Name the blood parasite species.
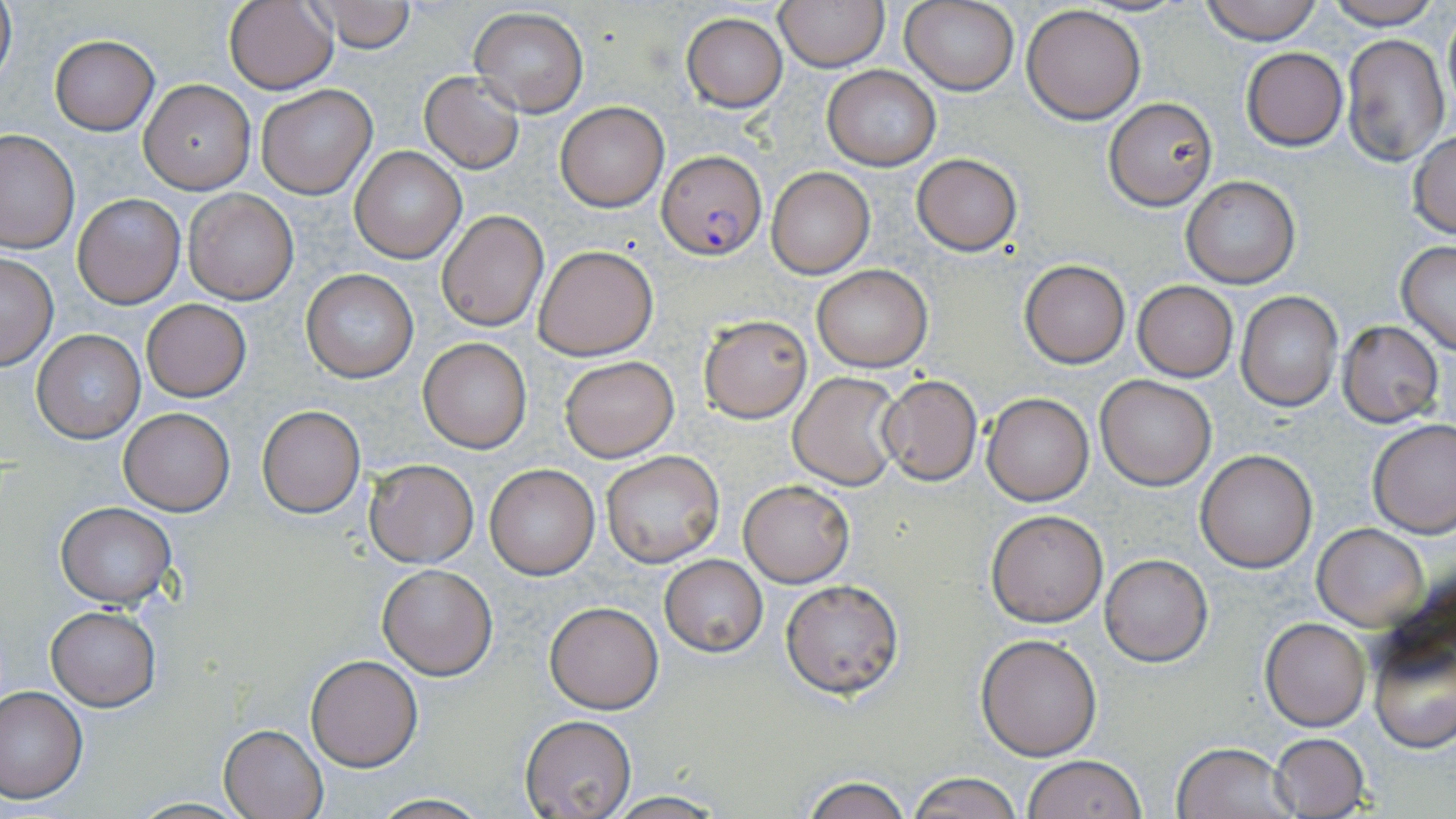
Plasmodium falciparum.

Approximate bounding boxes as named x1/y1/x2/y2 corners in pixels. Plasmodium falciparum-infected red blood cell locations: (x1=658, y1=149, x2=765, y2=260). Uninfected red blood cell locations: (x1=0, y1=0, x2=16, y2=90), (x1=223, y1=0, x2=339, y2=93), (x1=306, y1=0, x2=416, y2=52), (x1=774, y1=0, x2=889, y2=72), (x1=1198, y1=0, x2=1323, y2=44), (x1=1319, y1=0, x2=1442, y2=28), (x1=900, y1=1, x2=1019, y2=95), (x1=1022, y1=4, x2=1146, y2=123), (x1=469, y1=7, x2=589, y2=116), (x1=1441, y1=10, x2=1456, y2=115), (x1=680, y1=12, x2=788, y2=112), (x1=1340, y1=33, x2=1449, y2=166), (x1=50, y1=36, x2=158, y2=135), (x1=1241, y1=47, x2=1348, y2=150), (x1=822, y1=66, x2=942, y2=170), (x1=419, y1=71, x2=525, y2=174), (x1=140, y1=79, x2=256, y2=193), (x1=258, y1=84, x2=378, y2=199), (x1=1104, y1=98, x2=1217, y2=208), (x1=556, y1=102, x2=669, y2=212), (x1=0, y1=129, x2=78, y2=252), (x1=1407, y1=131, x2=1456, y2=237), (x1=349, y1=147, x2=466, y2=263), (x1=912, y1=154, x2=1020, y2=255), (x1=767, y1=167, x2=875, y2=278), (x1=1181, y1=175, x2=1300, y2=290), (x1=184, y1=189, x2=298, y2=304), (x1=73, y1=193, x2=184, y2=308), (x1=437, y1=210, x2=549, y2=331), (x1=1396, y1=241, x2=1456, y2=355), (x1=533, y1=244, x2=658, y2=359), (x1=0, y1=254, x2=58, y2=369), (x1=1021, y1=260, x2=1130, y2=367), (x1=812, y1=265, x2=931, y2=372), (x1=301, y1=269, x2=419, y2=383), (x1=1133, y1=281, x2=1238, y2=381), (x1=1236, y1=291, x2=1342, y2=411), (x1=141, y1=299, x2=251, y2=402), (x1=698, y1=314, x2=812, y2=423), (x1=1337, y1=322, x2=1442, y2=427), (x1=30, y1=329, x2=145, y2=444), (x1=418, y1=338, x2=532, y2=454), (x1=560, y1=356, x2=677, y2=461), (x1=789, y1=371, x2=903, y2=489), (x1=879, y1=375, x2=981, y2=486), (x1=1097, y1=375, x2=1217, y2=490), (x1=981, y1=392, x2=1094, y2=504), (x1=257, y1=404, x2=365, y2=518), (x1=119, y1=408, x2=234, y2=515), (x1=1368, y1=419, x2=1456, y2=537), (x1=1195, y1=450, x2=1318, y2=573), (x1=600, y1=451, x2=724, y2=567), (x1=364, y1=459, x2=479, y2=567), (x1=484, y1=463, x2=600, y2=580), (x1=740, y1=479, x2=853, y2=586), (x1=55, y1=502, x2=178, y2=606), (x1=985, y1=508, x2=1110, y2=628), (x1=1313, y1=523, x2=1429, y2=629), (x1=1100, y1=554, x2=1213, y2=667), (x1=660, y1=555, x2=767, y2=656), (x1=377, y1=564, x2=498, y2=679), (x1=779, y1=577, x2=905, y2=700), (x1=545, y1=602, x2=663, y2=713), (x1=46, y1=606, x2=161, y2=710), (x1=1260, y1=617, x2=1370, y2=731), (x1=976, y1=634, x2=1102, y2=760), (x1=1370, y1=637, x2=1455, y2=753), (x1=304, y1=655, x2=423, y2=772), (x1=0, y1=686, x2=88, y2=802), (x1=519, y1=715, x2=636, y2=819), (x1=219, y1=724, x2=327, y2=819), (x1=1267, y1=732, x2=1370, y2=819), (x1=1171, y1=741, x2=1298, y2=819), (x1=1023, y1=754, x2=1148, y2=819), (x1=907, y1=772, x2=1023, y2=819), (x1=799, y1=775, x2=912, y2=819), (x1=603, y1=793, x2=728, y2=818), (x1=365, y1=794, x2=494, y2=819). May-Grünwald-Giemsa stain. Captured at 1000x magnification. Light microscopy. One field of a larger specimen. Image is 1456×819 pixels. Thin blood film.